Assess this cell for malaria.
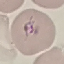
Parasitized.

Summary:
  - Preparation: thin blood smear
  - Capture: smartphone camera at the microscope eyepiece
  - Image type: cell patch, automatically extracted from a larger field of view and resized to 64 × 64 pixels
  - Stain: Giemsa